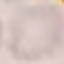

Summary:
  - Malaria status: uninfected
  - Stain: Giemsa
  - Image type: automatically extracted cell patch, resized to 64 × 64 pixels
  - Preparation: thin blood film
  - Capture: smartphone camera at the microscope eyepiece